Assess the morphology of the red blood cells.
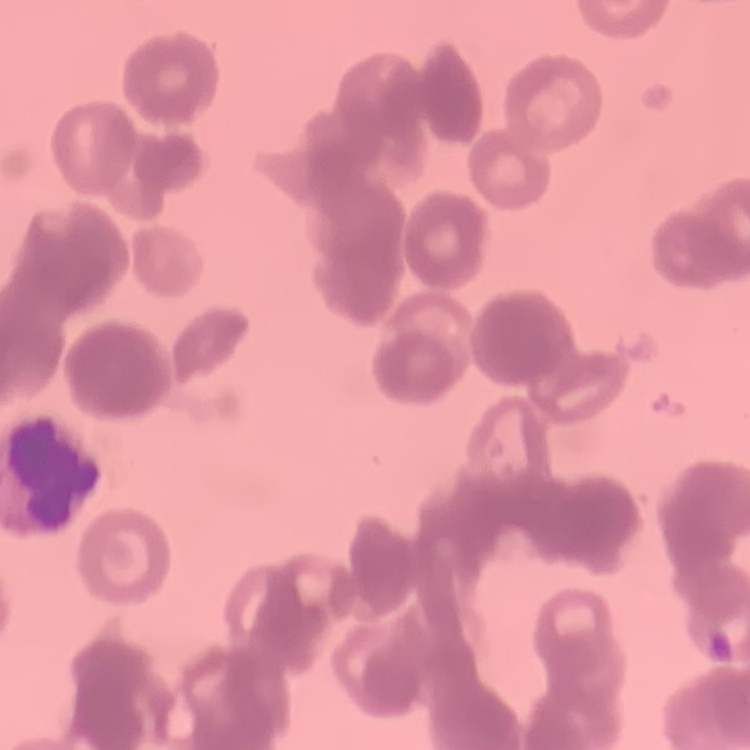
Rouleaux formation.

Summary:
  - Preparation: thin peripheral smear
  - Stain: Field's or Giemsa
  - Image type: one tile cut from a larger photomicrograph